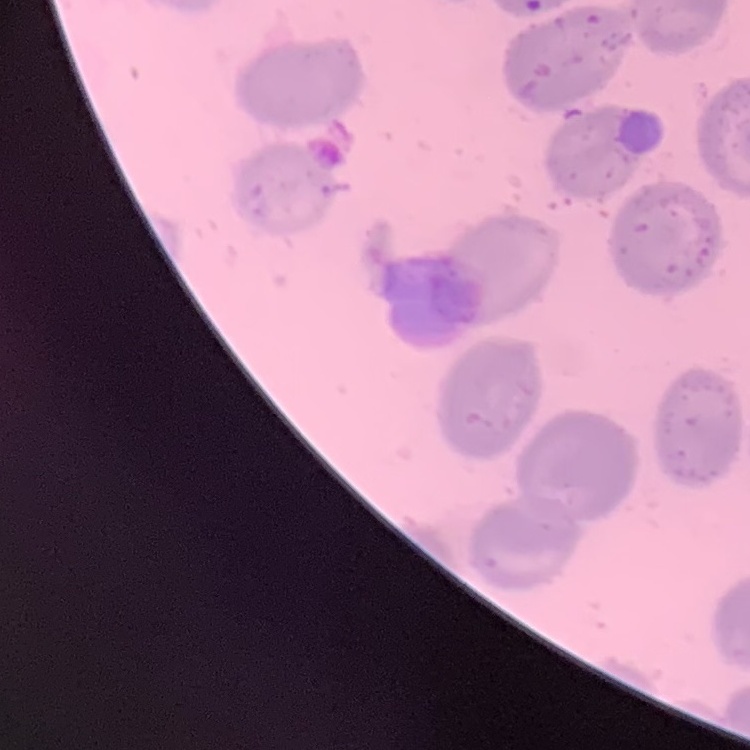 The red blood cells show no rouleaux formation. Thin peripheral smear. Field's or Giemsa stain. One tile cut from a larger photomicrograph.